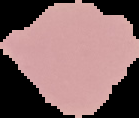

Result: no malaria parasites seen. Segmented cell region on a black background. From a thin blood film. Image is 139×118 pixels.